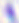

modality = photomicrograph
identification = Toxoplasma gondii
magnification = 400x